Point out each malaria parasite.
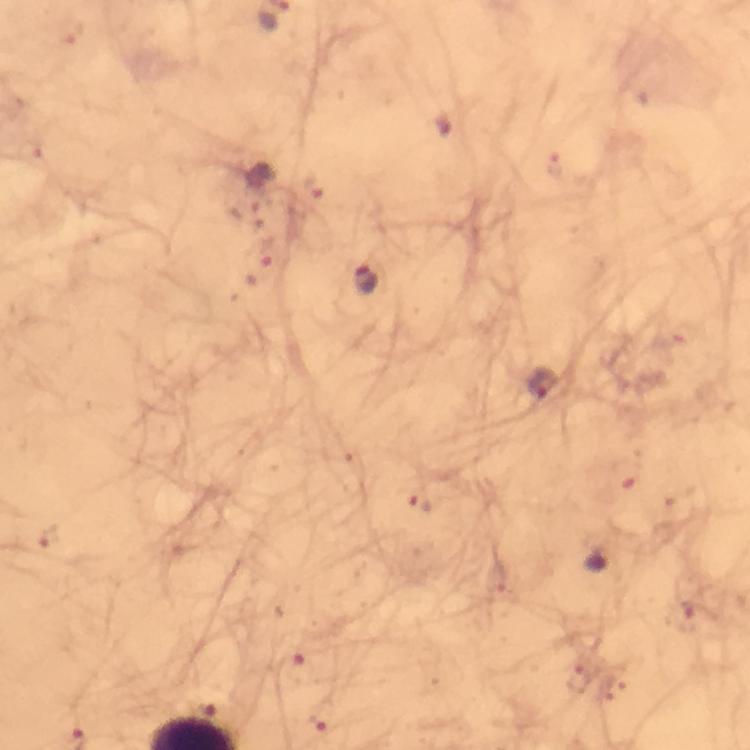
Approximate object centers, in pixels from the top-left corner.
Malaria parasites: (x=67, y=30), (x=446, y=121), (x=30, y=150), (x=555, y=164), (x=312, y=187), (x=250, y=203), (x=265, y=252), (x=364, y=279), (x=543, y=386), (x=628, y=474), (x=423, y=500), (x=48, y=535), (x=686, y=617), (x=296, y=667), (x=581, y=679), (x=327, y=719).

100x magnification. Immersion oil applied. Image is 750×750 pixels. Cropped region of a single field of view. Thick smear. Giemsa stain. From a diagnostic examination for malaria. Photographed through the microscope with a smartphone camera.